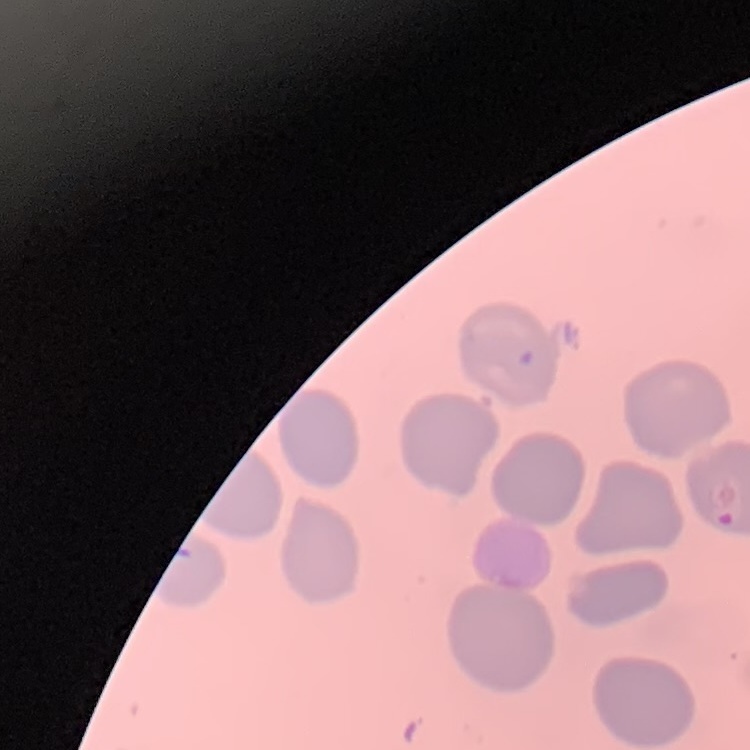
Summary:
  - Red blood cell morphology: no rouleaux formation
  - Preparation: thin blood smear
  - Image type: square crop of a larger photomicrograph
  - Stain: Field's or Giemsa